Name the parasite shown.
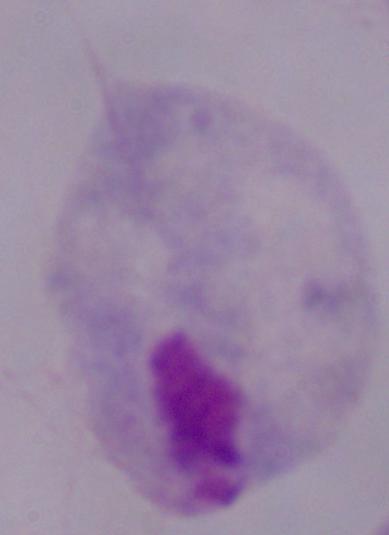

This is a trichomonad.

1000x magnification. Photomicrograph.